Find each parasitized red blood cell.
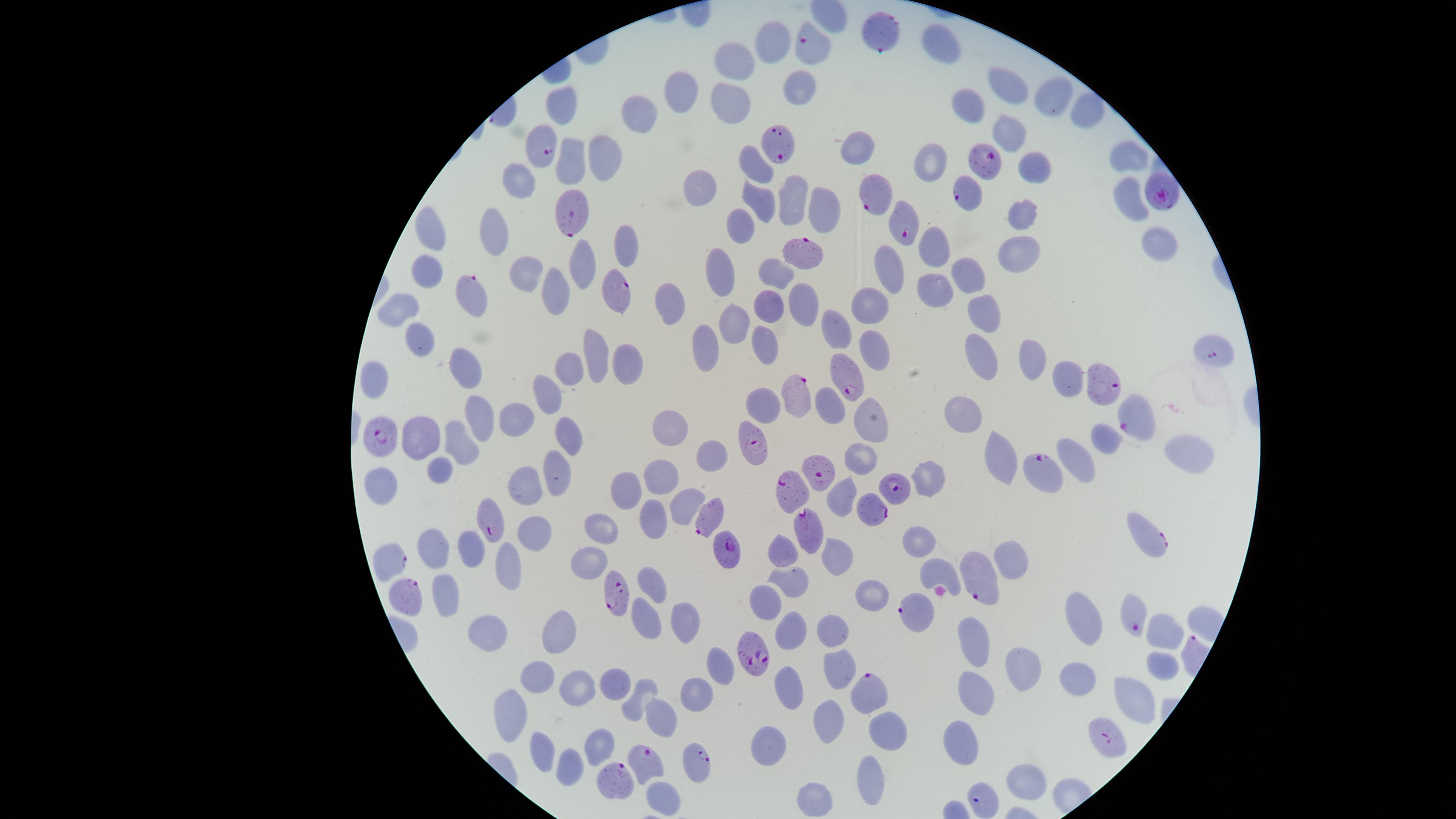
Approximate marker points as [x, y] in pixels.
Parasitized red blood cells: [881, 30], [806, 42], [776, 143], [543, 146], [985, 159], [880, 191], [1157, 192], [964, 194], [570, 210], [902, 223], [801, 252], [616, 293], [469, 297], [1215, 353], [844, 374], [1108, 382], [796, 395], [1136, 418], [382, 433], [752, 439], [1049, 470], [816, 473], [896, 489], [789, 491], [874, 507], [707, 511], [490, 519], [806, 527], [1147, 535], [731, 549], [388, 556], [981, 578], [616, 596], [408, 601], [911, 610], [1132, 616], [758, 653], [868, 694], [1103, 739], [644, 760], [701, 766], [616, 785], [980, 796].

Approximate marker points as [x, y] in pixels. Uninfected red blood cells: [771, 47], [943, 49], [736, 66], [1009, 87], [791, 90], [679, 94], [1053, 97], [729, 102], [559, 107], [971, 107], [1093, 111], [645, 117], [1007, 125], [859, 151], [1129, 156], [608, 158], [936, 161], [573, 163], [756, 163], [1032, 165], [521, 181], [707, 190], [1129, 197], [794, 199], [759, 201], [826, 210], [1021, 213], [738, 223], [496, 226], [437, 237], [936, 244], [1160, 245], [624, 246], [1015, 252], [726, 264], [578, 265], [429, 269], [529, 269], [889, 269], [967, 270], [776, 273], [932, 287], [550, 292], [770, 301], [803, 301], [407, 304], [670, 305], [872, 305], [986, 311], [732, 327], [839, 327], [416, 340], [710, 345], [764, 346], [877, 351], [978, 356], [597, 357], [1031, 359], [622, 362], [465, 366], [569, 371], [1065, 381], [375, 382], [549, 394], [762, 406], [828, 406], [966, 413], [481, 414], [512, 414], [868, 421], [672, 431], [566, 432], [1104, 437], [421, 438], [462, 441], [712, 452], [862, 452], [1185, 452], [1000, 454], [1076, 456], [438, 470], [554, 474], [932, 475], [660, 477], [385, 480], [526, 483], [627, 485], [840, 496], [682, 503], [649, 517], [536, 528], [603, 529], [918, 541], [785, 547], [437, 550], [473, 551], [838, 553], [509, 558], [1015, 561], [588, 563], [938, 570], [796, 580], [652, 582], [446, 593], [872, 595], [762, 601], [644, 616], [683, 617], [1086, 619], [836, 626], [486, 631], [789, 633], [1161, 634], [560, 635], [976, 644], [1159, 663], [723, 665], [1023, 666], [839, 669], [1076, 675], [541, 679], [579, 685], [620, 687], [696, 690], [977, 692], [1133, 695], [782, 696], [636, 700], [514, 712], [665, 715], [828, 719], [893, 730], [964, 735], [771, 741], [602, 747], [546, 753], [568, 771], [870, 777], [1024, 782], [657, 799], [819, 799]. Image is 1456×819 pixels. Single field of view. Giemsa stain. Circular visible region. Species: Plasmodium falciparum. Smartphone photograph through the microscope eyepiece. Thin blood film.